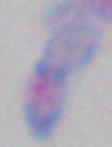

Summary:
  - Magnification: 1000x
  - Modality: photomicrograph
  - Identification: Toxoplasma gondii